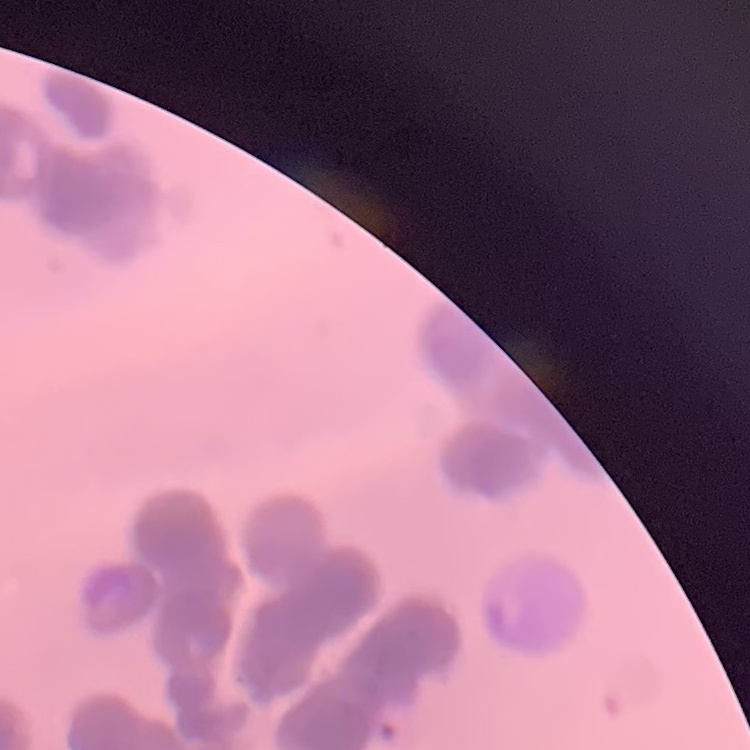
Summary:
  - Erythrocyte morphology: rouleaux formation
  - Preparation: thin peripheral smear
  - Image type: one tile cut from a larger photomicrograph
  - Stain: Field's or Giemsa